Classify this cell by malaria status.
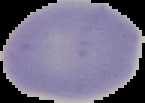

It is uninfected.

Image is 145×103 pixels. Segmented cell region on a black background. From a thin blood smear.